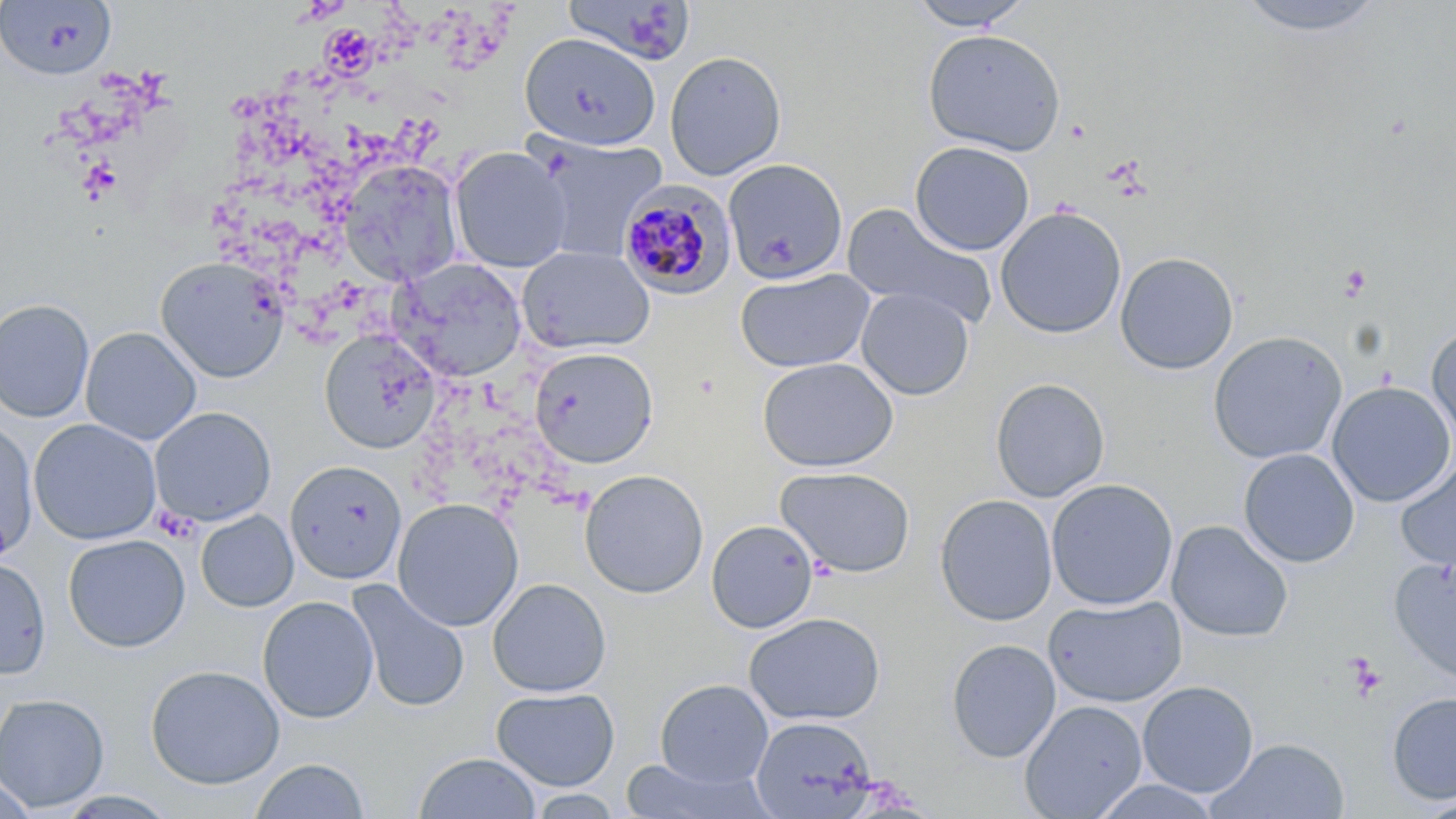
Approximate bounding boxes as [x1, y1, x2, y2] in pixels. Platelet locations: [1338, 263, 1372, 301], [155, 507, 201, 546], [1345, 653, 1386, 700]. Plasmodium malariae-infected red blood cell locations: [618, 179, 737, 300]. Uninfected red blood cell locations: [906, 0, 1035, 31], [1233, 0, 1390, 38], [1, 1, 116, 80], [563, 1, 698, 66], [922, 29, 1067, 156], [519, 32, 661, 152], [665, 50, 786, 180], [531, 135, 668, 262], [909, 141, 1035, 255], [450, 146, 571, 272], [722, 158, 848, 284], [338, 159, 464, 285], [842, 203, 998, 331], [995, 206, 1127, 339], [517, 247, 655, 355], [1115, 251, 1239, 375], [155, 256, 291, 382], [392, 258, 527, 381], [735, 268, 875, 373], [856, 287, 974, 400], [0, 298, 95, 422], [1426, 325, 1456, 448], [80, 327, 201, 445], [319, 330, 442, 454], [1207, 331, 1348, 464], [529, 347, 658, 467], [757, 357, 899, 472], [990, 378, 1111, 502], [1327, 382, 1455, 507], [149, 407, 276, 527], [28, 418, 161, 544], [0, 421, 38, 559], [1238, 448, 1360, 568], [285, 460, 407, 585], [1395, 460, 1456, 573], [775, 466, 916, 578], [579, 469, 709, 598], [1046, 478, 1179, 611], [935, 494, 1058, 626], [392, 498, 524, 631], [196, 510, 299, 612], [706, 519, 819, 633], [1166, 520, 1293, 643], [63, 534, 190, 652], [0, 556, 50, 679], [1389, 556, 1456, 686], [488, 578, 611, 697], [348, 580, 471, 714], [257, 595, 378, 723], [1045, 595, 1187, 708], [744, 612, 886, 726], [945, 638, 1061, 762], [145, 663, 285, 789], [654, 678, 774, 788], [1137, 680, 1259, 798], [490, 687, 620, 790], [1386, 691, 1456, 805], [0, 693, 110, 812], [1019, 699, 1148, 818], [749, 715, 879, 817], [1207, 737, 1351, 819], [414, 752, 541, 818], [250, 758, 370, 818], [620, 758, 771, 819], [0, 771, 39, 818], [1090, 778, 1225, 818], [526, 789, 626, 818], [1410, 793, 1456, 819]. Slide-level diagnosis: Plasmodium malariae. May-Grünwald-Giemsa stain. Image is 1456×819 pixels. Optical microscopy. Single field of view. 1000x magnification. Thin blood film.